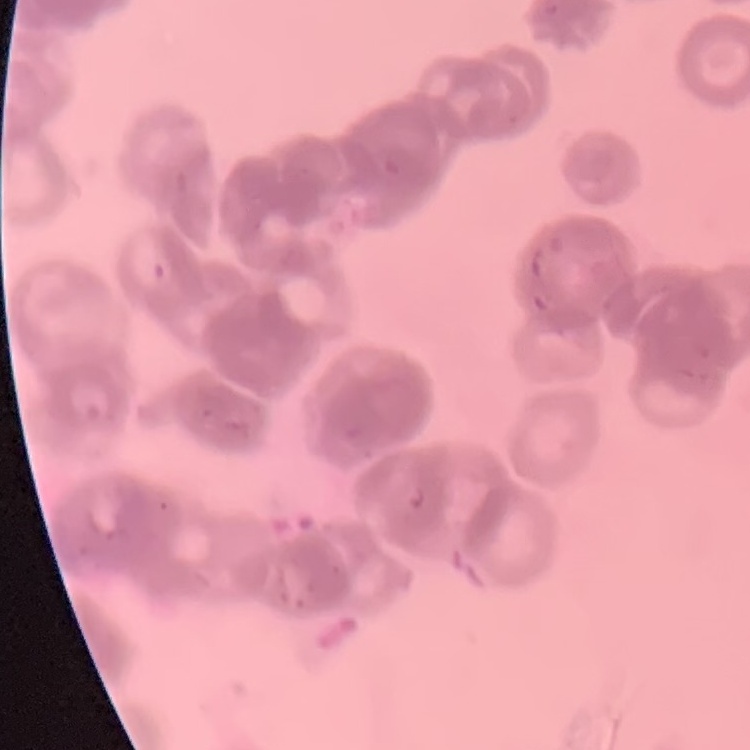
erythrocyte morphology = rouleaux formation
stain = Field's or Giemsa
preparation = thin blood smear
image type = square crop of a larger photomicrograph